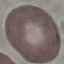
Summary:
  - Result: no malaria parasites detected
  - Stain: Giemsa
  - Preparation: thin blood smear
  - Image type: cell patch, automatically extracted from a larger field of view and resized to 64 × 64 pixels
  - Capture: smartphone camera at the microscope eyepiece